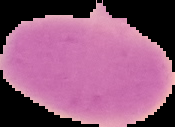
preparation: thin blood film
image_size: 175×127 pixels
result: no Plasmodium parasites seen
image_type: segmented cell region on a black background